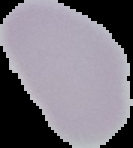

From a thin blood film. Malaria status: uninfected. The area outside the segmented cell region is set to black. Image is 133×148 pixels.